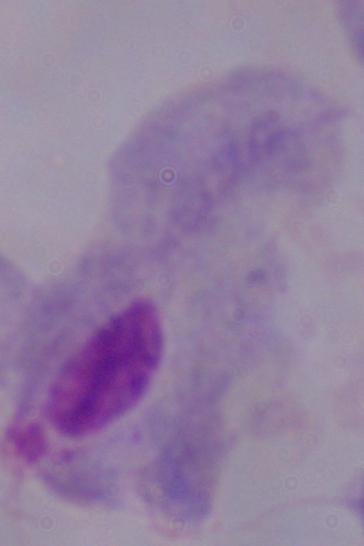

modality = micrograph
magnification = 1000x
identification = trichomonad